Mark where cells are.
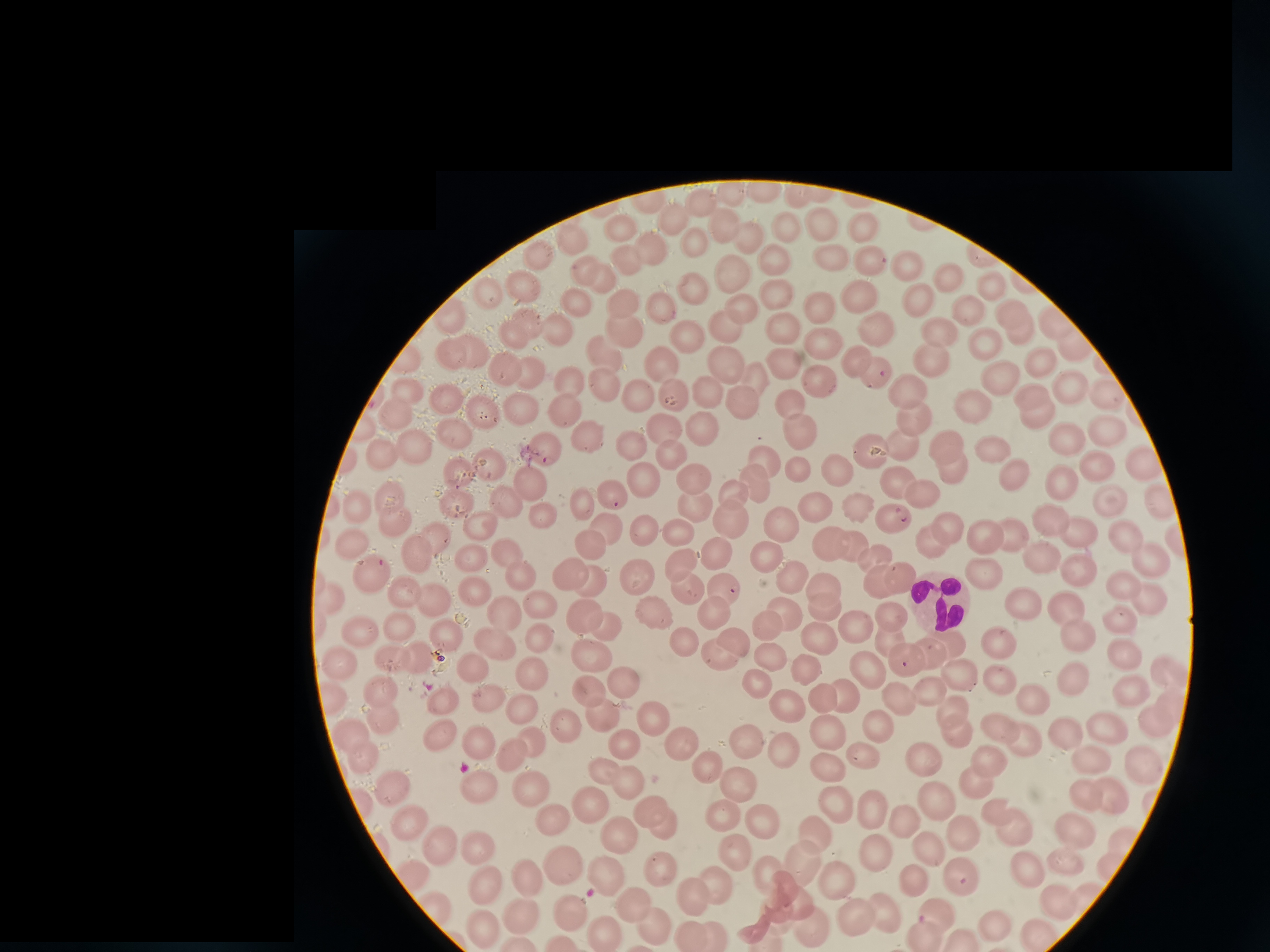
Approximate centers as {x, y} in pixels.
Cells: {764, 192}, {729, 194}, {795, 196}, {702, 202}, {674, 219}, {823, 223}, {863, 224}, {722, 225}, {621, 228}, {784, 231}, {749, 237}, {570, 239}, {693, 241}, {649, 245}, {537, 258}, {770, 258}, {830, 258}, {867, 259}, {625, 263}, {909, 264}, {583, 269}, {732, 274}, {604, 277}, {951, 277}, {522, 285}, {693, 286}, {993, 287}, {776, 291}, {858, 293}, {490, 294}, {922, 300}, {621, 303}, {581, 305}, {816, 308}, {659, 309}, {743, 310}, {969, 310}, {449, 317}, {1055, 322}, {1016, 324}, {533, 326}, {725, 326}, {558, 329}, {878, 329}, {624, 330}, {781, 331}, {686, 332}, {516, 335}, {943, 338}, {989, 344}, {1071, 346}, {825, 348}, {449, 351}, {467, 355}, {602, 356}, {929, 357}, {857, 358}, {782, 359}, {728, 361}, {663, 362}, {1042, 364}, {504, 371}, {532, 371}, {874, 374}, {755, 376}, {998, 379}, {820, 381}, {566, 382}, {605, 387}, {908, 390}, {1071, 390}, {708, 391}, {408, 392}, {673, 394}, {1034, 394}, {447, 397}, {641, 397}, {1109, 397}, {737, 398}, {788, 400}, {969, 402}, {565, 406}, {519, 408}, {482, 410}, {912, 417}, {1037, 417}, {393, 418}, {702, 426}, {665, 429}, {1107, 432}, {801, 434}, {451, 435}, {586, 436}, {628, 442}, {1068, 442}, {947, 444}, {899, 445}, {992, 448}, {415, 449}, {545, 450}, {869, 450}, {671, 453}, {384, 456}, {763, 460}, {1092, 462}, {1143, 463}, {491, 466}, {797, 471}, {1010, 472}, {951, 473}, {456, 474}, {837, 474}, {534, 477}, {690, 478}, {894, 479}, {642, 480}, {1058, 480}, {755, 483}, {607, 491}, {921, 492}, {732, 494}, {1158, 496}, {503, 497}, {393, 499}, {581, 500}, {455, 501}, {1109, 502}, {692, 505}, {813, 505}, {854, 507}, {358, 510}, {542, 516}, {889, 516}, {1054, 517}, {393, 520}, {731, 520}, {779, 521}, {481, 523}, {948, 524}, {645, 525}, {606, 528}, {678, 529}, {1073, 530}, {1009, 533}, {983, 534}, {1130, 536}, {435, 537}, {932, 540}, {828, 541}, {587, 542}, {850, 543}, {356, 544}, {507, 550}, {416, 555}, {475, 556}, {715, 556}, {762, 557}, {1042, 557}, {1145, 557}, {875, 558}, {681, 565}, {568, 570}, {1080, 571}, {634, 572}, {980, 572}, {371, 573}, {788, 575}, {899, 575}, {525, 576}, {879, 578}, {591, 579}, {823, 584}, {1122, 584}, {686, 586}, {475, 587}, {723, 587}, {402, 589}, {330, 596}, {1146, 598}, {435, 602}, {542, 604}, {1024, 605}, {1067, 606}, {825, 608}, {656, 609}, {716, 609}, {585, 610}, {786, 613}, {891, 614}, {505, 615}, {1119, 622}, {404, 623}, {607, 625}, {768, 627}, {859, 628}, {358, 629}, {1075, 634}, {889, 635}, {731, 637}, {539, 638}, {817, 638}, {493, 639}, {999, 640}, {684, 641}, {453, 642}, {948, 645}, {588, 650}, {717, 650}, {928, 652}, {767, 655}, {417, 656}, {1121, 656}, {394, 658}, {340, 659}, {903, 659}, {804, 664}, {476, 666}, {864, 667}, {536, 668}, {959, 672}, {1168, 674}, {755, 678}, {995, 678}, {626, 682}, {1072, 682}, {383, 688}, {927, 688}, {1130, 688}, {592, 689}, {843, 694}, {817, 695}, {326, 699}, {1030, 699}, {445, 700}, {487, 700}, {897, 702}, {788, 709}, {523, 710}, {1173, 710}, {383, 714}, {603, 714}, {654, 717}, {955, 717}, {567, 722}, {997, 722}, {1154, 725}, {874, 726}, {1109, 728}, {1064, 732}, {825, 733}, {344, 735}, {446, 737}, {1022, 737}, {482, 739}, {679, 739}, {747, 742}, {535, 743}, {622, 743}, {512, 753}, {788, 756}, {865, 756}, {989, 756}, {363, 757}, {1090, 757}, {922, 760}, {1141, 761}, {707, 763}, {826, 767}, {615, 776}, {739, 780}, {975, 780}, {475, 782}, {528, 785}, {394, 790}, {1082, 793}, {1109, 795}, {592, 796}, {938, 800}, {835, 802}, {868, 806}, {999, 807}, {551, 810}, {724, 816}, {762, 817}, {657, 819}, {901, 821}, {412, 823}, {1009, 823}, {1069, 828}, {815, 829}, {619, 831}, {962, 833}, {923, 845}, {481, 850}, {742, 850}, {438, 851}, {873, 853}, {1066, 861}, {803, 863}, {1023, 864}, {564, 865}, {662, 871}, {412, 873}, {771, 873}, {829, 873}, {528, 875}, {604, 876}, {959, 876}, {915, 879}, {717, 881}, {485, 883}, {695, 898}, {1055, 898}, {637, 903}, {437, 906}, {885, 907}, {573, 909}, {518, 912}, {940, 913}, {857, 914}, {991, 916}.

{
  "image_size": "1270×952 pixels",
  "preparation": "thin smear",
  "field_of_view": "single",
  "capture": "smartphone camera at the microscope eyepiece",
  "stain": "Giemsa"
}